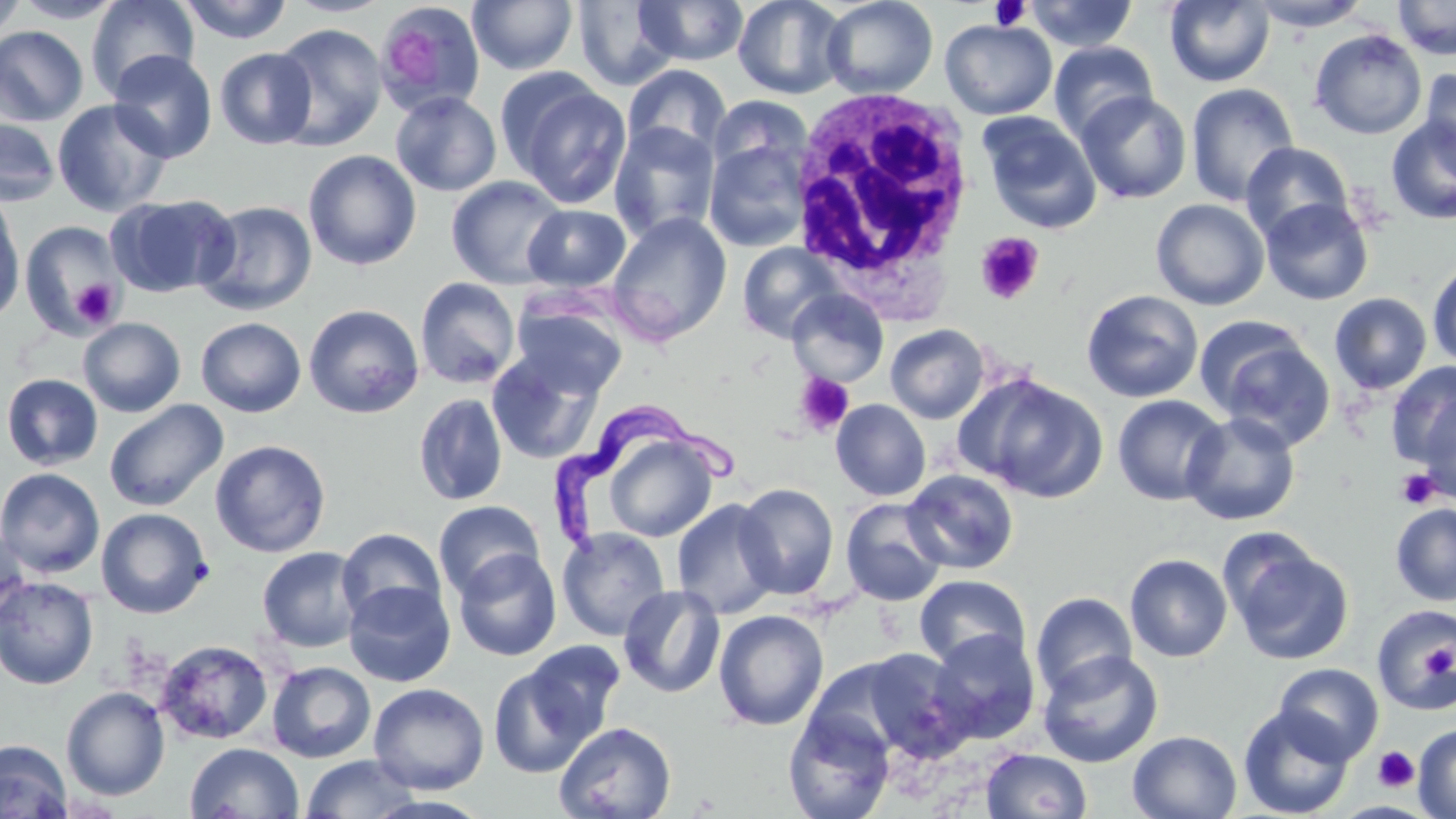

slide-level diagnosis = Trypanosoma brucei
modality = optical microscopy
image size = 1456×819 pixels
Trypanosoma brucei locations = approximate bounding boxes as (x1,y1)-(x2,y2) corner pairs in pixels: (554,392)-(736,549)
uninfected red blood cell locations = approximate bounding boxes as (x1,y1)-(x2,y2) corner pairs in pixels: (0,0)-(28,44), (12,0)-(126,23), (85,0)-(199,98), (176,0)-(293,44), (283,0)-(394,17), (634,0)-(749,66), (732,0)-(849,99), (821,0)-(938,99), (1393,0)-(1456,59), (468,1)-(578,75), (571,1)-(680,91), (1023,1)-(1139,52), (1164,1)-(1275,87), (1246,1)-(1373,31), (375,3)-(485,117), (940,19)-(1057,120), (270,23)-(388,150), (0,26)-(89,126), (1309,28)-(1428,140), (1049,41)-(1159,143), (214,47)-(317,149), (108,50)-(217,162), (622,64)-(732,161), (1419,66)-(1456,178), (502,74)-(632,210), (1186,83)-(1299,206), (390,90)-(502,197), (1076,91)-(1192,204), (708,94)-(812,180), (52,99)-(173,217), (977,112)-(1102,233), (1385,114)-(1456,225), (0,115)-(62,207), (609,122)-(721,243), (704,139)-(811,252), (1240,141)-(1354,243), (303,149)-(422,270), (446,175)-(569,289), (106,194)-(239,298), (1,197)-(26,322), (1260,198)-(1374,305), (1151,199)-(1270,311), (195,200)-(317,316), (523,204)-(630,292), (606,211)-(732,346), (19,220)-(124,337), (737,242)-(845,343), (1427,260)-(1456,370), (415,277)-(521,389), (1081,289)-(1204,403), (787,290)-(889,387), (1329,292)-(1432,395), (510,301)-(628,399), (303,304)-(425,419), (78,317)-(186,417), (196,317)-(306,418), (885,324)-(990,424), (1202,328)-(1337,450), (486,349)-(605,465), (1386,362)-(1456,469), (0,373)-(104,471), (963,374)-(1107,502), (413,392)-(508,506), (1112,394)-(1229,506), (1417,398)-(1456,503), (104,399)-(228,512), (831,399)-(931,501), (1181,412)-(1301,525), (599,433)-(720,543), (210,439)-(331,558), (0,467)-(105,578), (901,469)-(1020,575), (735,483)-(839,600), (672,498)-(781,620), (840,498)-(948,606), (433,500)-(545,601), (1390,503)-(1456,606), (95,507)-(213,618), (337,527)-(446,625), (557,527)-(671,641), (0,529)-(31,632), (1221,533)-(1354,666), (256,546)-(366,653), (453,548)-(562,661), (1125,553)-(1233,662), (914,574)-(1030,671), (0,575)-(99,690), (343,581)-(456,687), (618,584)-(726,698), (1030,591)-(1138,699), (1371,604)-(1456,714), (713,609)-(829,730), (927,628)-(1041,745), (155,640)-(273,745), (522,640)-(626,744), (850,648)-(970,761), (1037,650)-(1164,768), (267,661)-(376,763), (488,662)-(601,779), (1273,662)-(1383,764), (368,682)-(490,795), (61,686)-(170,801), (1238,705)-(1355,819), (783,708)-(895,819), (553,721)-(677,819), (1413,724)-(1456,818), (1128,730)-(1243,819), (0,739)-(74,819), (184,742)-(304,818), (981,749)-(1092,819), (300,753)-(419,818)
stain = May-Grünwald-Giemsa
white blood cell locations = approximate bounding boxes as (x1,y1)-(x2,y2) corner pairs in pixels: (789,84)-(976,300)
preparation = thin blood film
platelet locations = approximate bounding boxes as (x1,y1)-(x2,y2) corner pairs in pixels: (987,1)-(1033,31), (383,30)-(438,86), (975,233)-(1045,305), (70,278)-(120,328), (794,373)-(854,436), (1395,468)-(1441,509), (1422,645)-(1455,679), (1373,747)-(1419,793)
magnification = 1000x
field of view = single